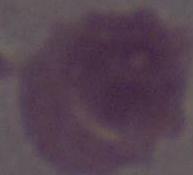
Captured at 1000x magnification. A red blood cell is seen. Micrograph.